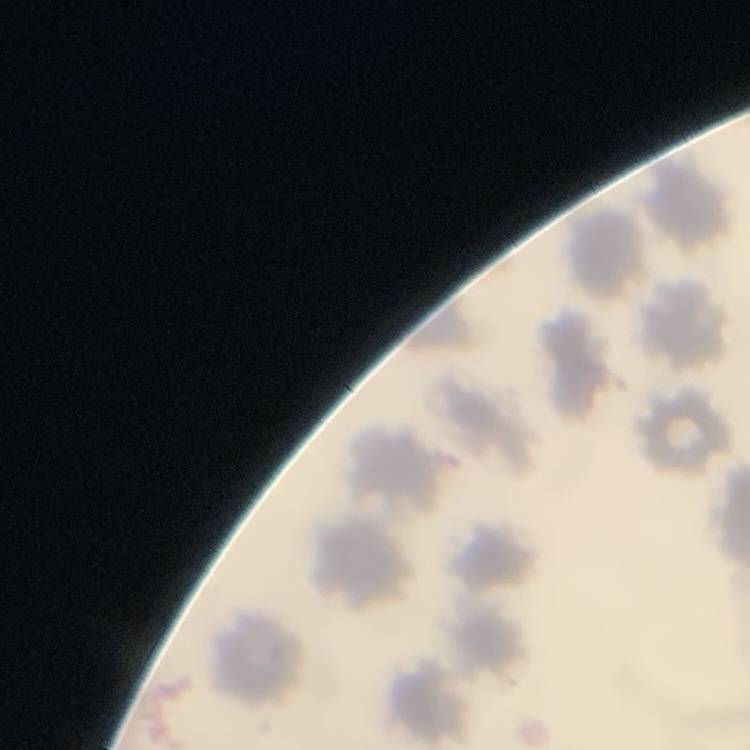

{
  "erythrocyte_morphology": "no rouleaux formation",
  "stain": "Field's or Giemsa",
  "image_type": "square crop of a larger photomicrograph",
  "preparation": "thin peripheral smear"
}